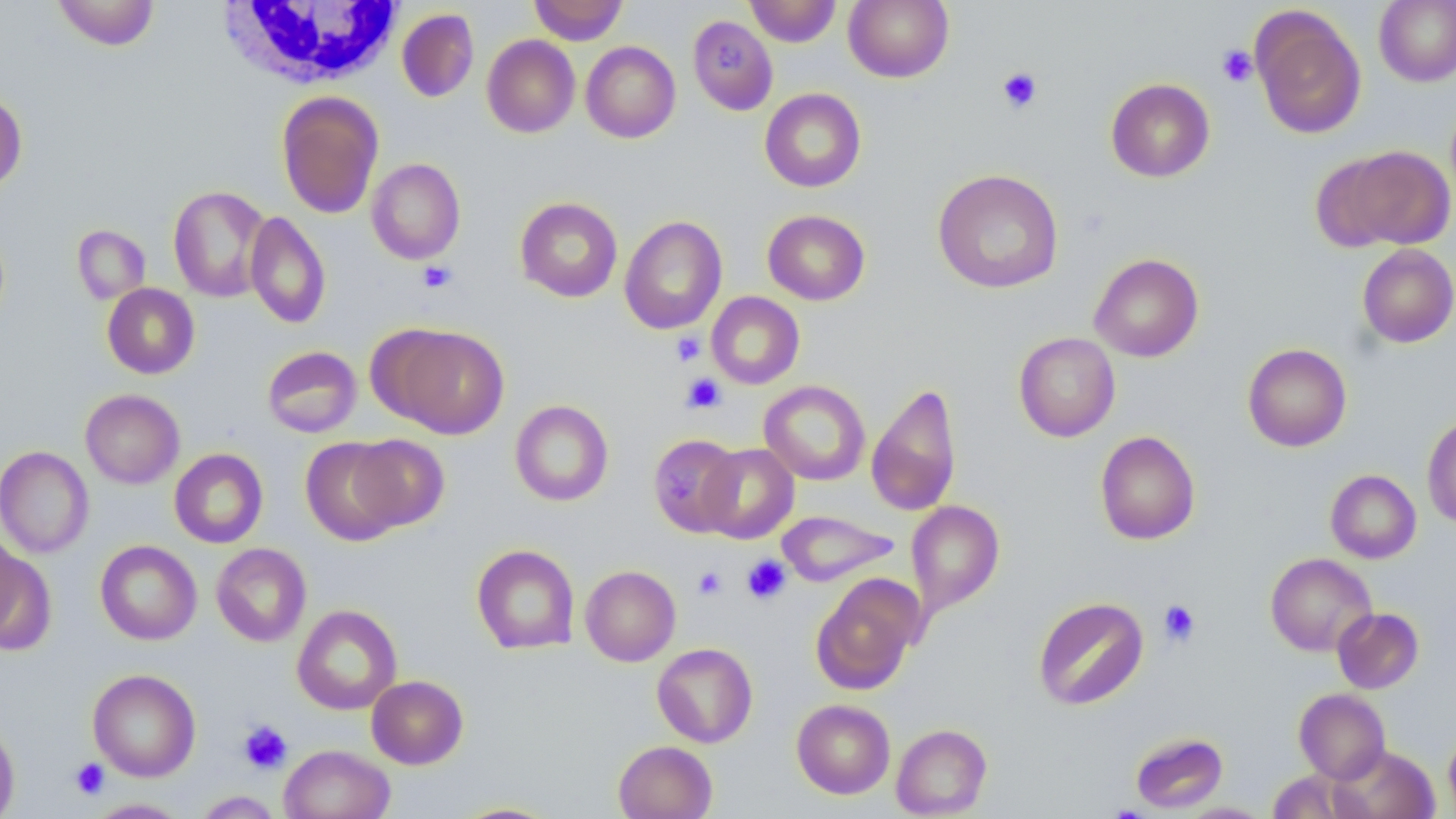

Summary:
  - Coordinate format: approximate bounding boxes as named x1/y1/x2/y2 corners in pixels
  - White blood cell locations: (x1=219, y1=0, x2=406, y2=91)
  - Uninfected red blood cell locations: (x1=51, y1=0, x2=161, y2=50), (x1=529, y1=0, x2=628, y2=45), (x1=744, y1=0, x2=841, y2=47), (x1=844, y1=0, x2=953, y2=83), (x1=1374, y1=0, x2=1456, y2=87), (x1=1250, y1=6, x2=1367, y2=139), (x1=397, y1=8, x2=479, y2=103), (x1=687, y1=15, x2=778, y2=116), (x1=482, y1=35, x2=580, y2=137), (x1=581, y1=41, x2=681, y2=143), (x1=1105, y1=78, x2=1215, y2=182), (x1=759, y1=88, x2=867, y2=192), (x1=0, y1=89, x2=27, y2=193), (x1=276, y1=90, x2=384, y2=219), (x1=1325, y1=145, x2=1455, y2=251), (x1=367, y1=158, x2=465, y2=264), (x1=932, y1=168, x2=1064, y2=294), (x1=168, y1=185, x2=272, y2=302), (x1=515, y1=196, x2=623, y2=302), (x1=762, y1=209, x2=870, y2=305), (x1=245, y1=211, x2=331, y2=328), (x1=619, y1=215, x2=727, y2=334), (x1=72, y1=225, x2=150, y2=304), (x1=1357, y1=243, x2=1456, y2=348), (x1=1089, y1=253, x2=1204, y2=362), (x1=102, y1=283, x2=200, y2=379), (x1=706, y1=292, x2=805, y2=389), (x1=381, y1=323, x2=510, y2=438), (x1=1014, y1=332, x2=1121, y2=442), (x1=1242, y1=343, x2=1352, y2=452), (x1=261, y1=346, x2=362, y2=438), (x1=759, y1=380, x2=870, y2=486), (x1=866, y1=381, x2=962, y2=517), (x1=80, y1=389, x2=184, y2=489), (x1=510, y1=400, x2=613, y2=506), (x1=1422, y1=413, x2=1456, y2=529), (x1=1095, y1=430, x2=1200, y2=545), (x1=349, y1=434, x2=450, y2=534), (x1=649, y1=434, x2=744, y2=538), (x1=301, y1=437, x2=408, y2=544), (x1=698, y1=443, x2=798, y2=543), (x1=0, y1=445, x2=94, y2=558), (x1=169, y1=448, x2=268, y2=548), (x1=1326, y1=469, x2=1422, y2=563), (x1=906, y1=500, x2=1004, y2=615), (x1=776, y1=510, x2=899, y2=586), (x1=0, y1=528, x2=26, y2=644), (x1=0, y1=540, x2=55, y2=653), (x1=95, y1=540, x2=202, y2=645), (x1=211, y1=543, x2=311, y2=646), (x1=471, y1=544, x2=580, y2=654), (x1=1265, y1=552, x2=1377, y2=656), (x1=580, y1=565, x2=680, y2=666), (x1=811, y1=575, x2=922, y2=695), (x1=1033, y1=596, x2=1148, y2=710), (x1=292, y1=604, x2=402, y2=714), (x1=1332, y1=607, x2=1424, y2=693), (x1=652, y1=643, x2=758, y2=747), (x1=87, y1=668, x2=201, y2=781), (x1=366, y1=675, x2=468, y2=769), (x1=1294, y1=688, x2=1391, y2=784), (x1=792, y1=699, x2=895, y2=799), (x1=0, y1=717, x2=20, y2=819), (x1=891, y1=723, x2=992, y2=817), (x1=1443, y1=727, x2=1456, y2=817), (x1=1129, y1=731, x2=1229, y2=813), (x1=613, y1=740, x2=718, y2=819), (x1=279, y1=744, x2=395, y2=819), (x1=1329, y1=744, x2=1439, y2=819), (x1=1266, y1=770, x2=1354, y2=817), (x1=192, y1=791, x2=284, y2=818), (x1=85, y1=798, x2=191, y2=818), (x1=448, y1=801, x2=564, y2=818), (x1=1178, y1=802, x2=1273, y2=818)
  - Platelet locations: (x1=1217, y1=45, x2=1258, y2=87), (x1=997, y1=67, x2=1043, y2=113), (x1=418, y1=261, x2=457, y2=293), (x1=671, y1=331, x2=705, y2=366), (x1=681, y1=373, x2=726, y2=413), (x1=741, y1=555, x2=791, y2=605), (x1=693, y1=566, x2=727, y2=600), (x1=1158, y1=599, x2=1201, y2=647), (x1=237, y1=720, x2=293, y2=774), (x1=70, y1=757, x2=110, y2=800)
  - Slide-level diagnosis: no evidence of blood parasites
  - Stain: May-Grünwald-Giemsa
  - Magnification: 1000x
  - Field of view: one of a larger specimen
  - Modality: light microscopy
  - Preparation: thin blood smear
  - Image size: 1456×819 pixels